Report the malaria status of this cell.
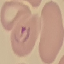

Parasitized.

Summary:
  - Capture: smartphone camera at the microscope eyepiece
  - Stain: Giemsa
  - Preparation: thin blood smear
  - Image type: automatically extracted cell patch, resized to 64 × 64 pixels